State which parasite is depicted.
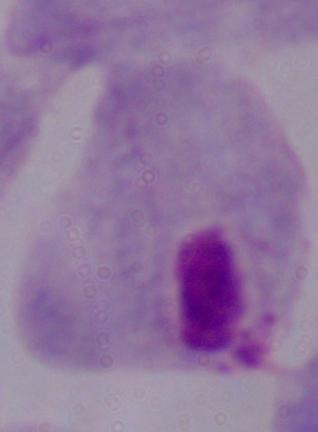

A trichomonad.

Summary:
  - Magnification: 1000x
  - Modality: micrograph